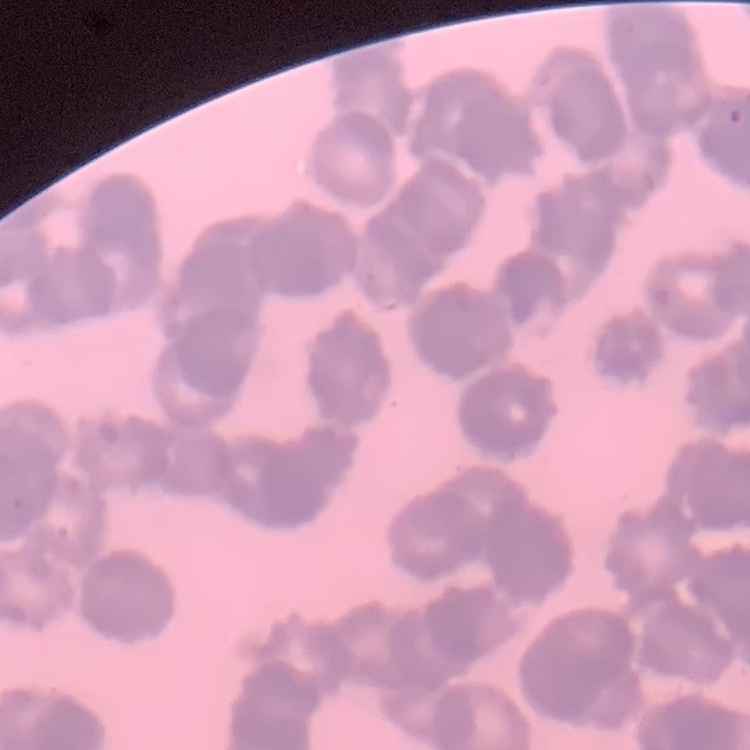

Summary:
  - Erythrocyte morphology: rouleaux formation
  - Stain: Field's or Giemsa
  - Preparation: thin peripheral smear
  - Image type: one tile cut from a larger photomicrograph